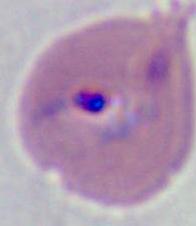

Photomicrograph. A Plasmodium parasite is shown. 400x or 1000x magnification.